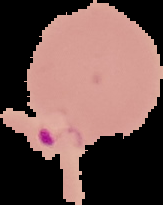

The area outside the segmented cell region is set to black. From a thin blood film. Result: malaria parasites identified. Image is 163×205 pixels.